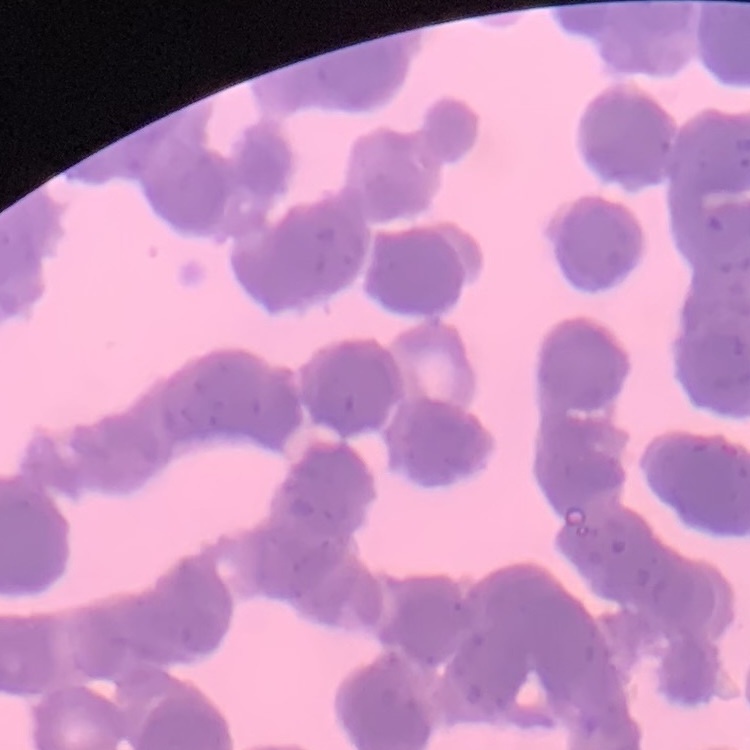

red blood cell morphology = rouleaux formation
image type = square crop of a larger photomicrograph
stain = Field's or Giemsa
preparation = thin blood film